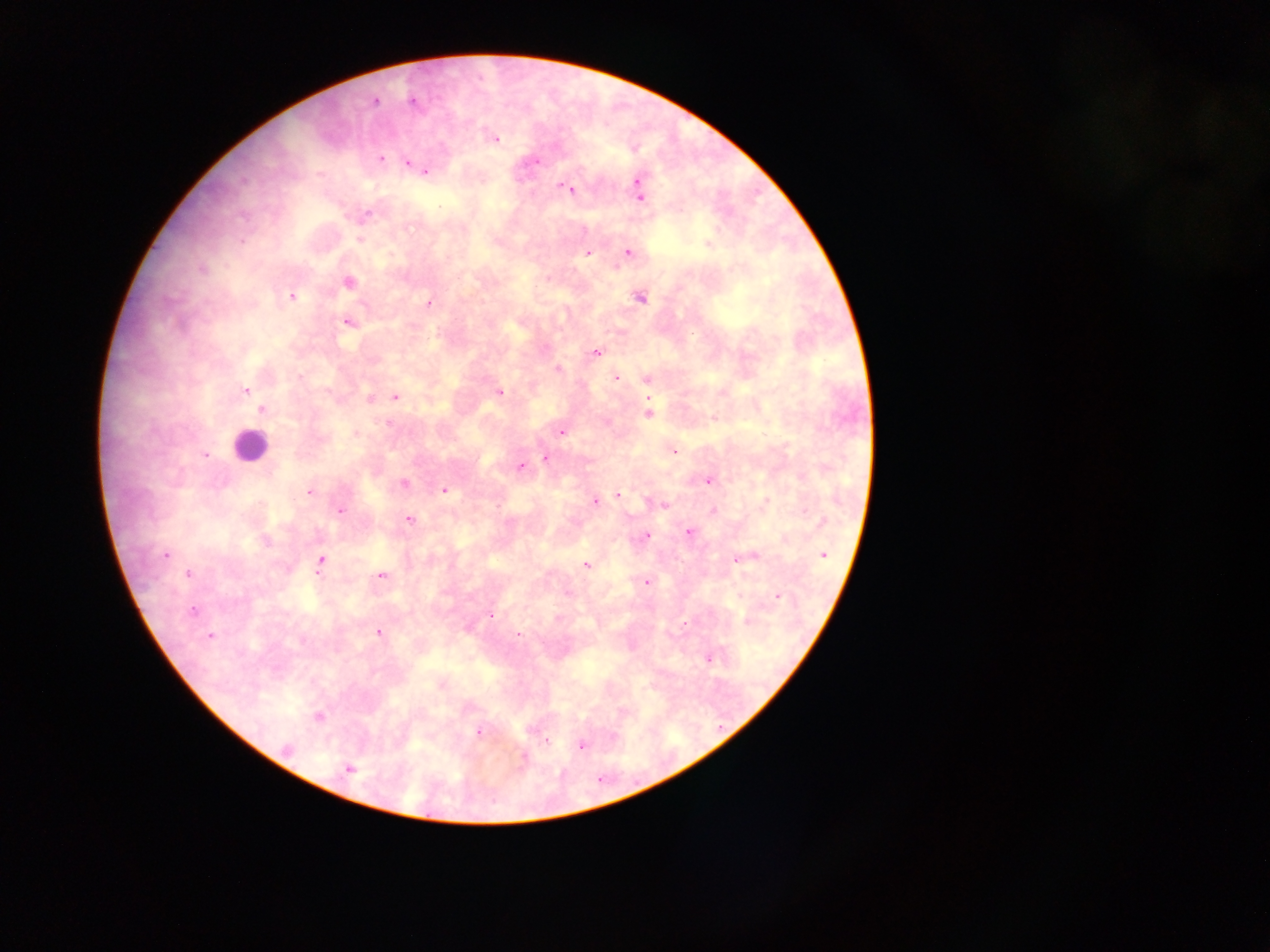

image size = 1270×952 pixels
malaria parasite locations = approximate centers as (x, y) in pixels: (374, 101), (412, 101), (494, 138), (380, 158), (534, 161), (408, 162), (413, 165), (425, 170), (567, 188), (639, 193), (360, 239), (627, 251), (587, 252), (348, 282), (290, 296), (639, 296), (428, 303), (347, 321), (595, 352), (558, 369), (616, 377), (647, 377), (245, 390), (498, 392), (395, 397), (369, 398), (261, 410), (648, 413), (561, 431), (673, 450), (203, 454), (545, 458), (520, 466), (709, 479), (403, 483), (444, 490), (309, 491), (618, 495), (594, 502), (662, 504), (339, 510), (712, 510), (408, 519), (688, 532), (644, 535), (165, 554), (823, 554), (740, 557), (320, 560), (586, 565), (188, 574), (380, 576), (646, 581), (776, 596), (192, 610), (490, 613), (747, 621), (467, 628), (378, 632), (518, 635), (210, 636), (708, 658), (441, 684), (318, 716), (480, 731), (544, 741), (581, 744), (286, 748), (523, 758), (349, 769)
capture = mobile-phone photograph through a microscope
country = Ghana
leukocyte locations = approximate centers as (x, y) in pixels: (249, 446)
field of view = single
preparation = thick blood film